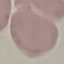

malaria status = uninfected
stain = Giemsa
preparation = thin blood film
image type = automatically extracted cell patch, resized to 64 × 64 pixels
capture = smartphone through the microscope eyepiece